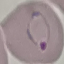

Summary:
  - Malaria status: parasitized
  - Image type: cell patch, automatically extracted from a larger field of view and resized to 64 × 64 pixels
  - Preparation: thin blood film
  - Capture: smartphone through the microscope eyepiece
  - Stain: Giemsa